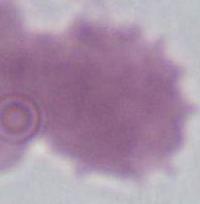

identification: red blood cell
magnification: 1000x
modality: photomicrograph